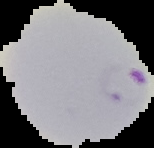
result = Plasmodium parasites identified
image size = 154×148 pixels
preparation = thin blood film
image type = segmented cell region on a black background